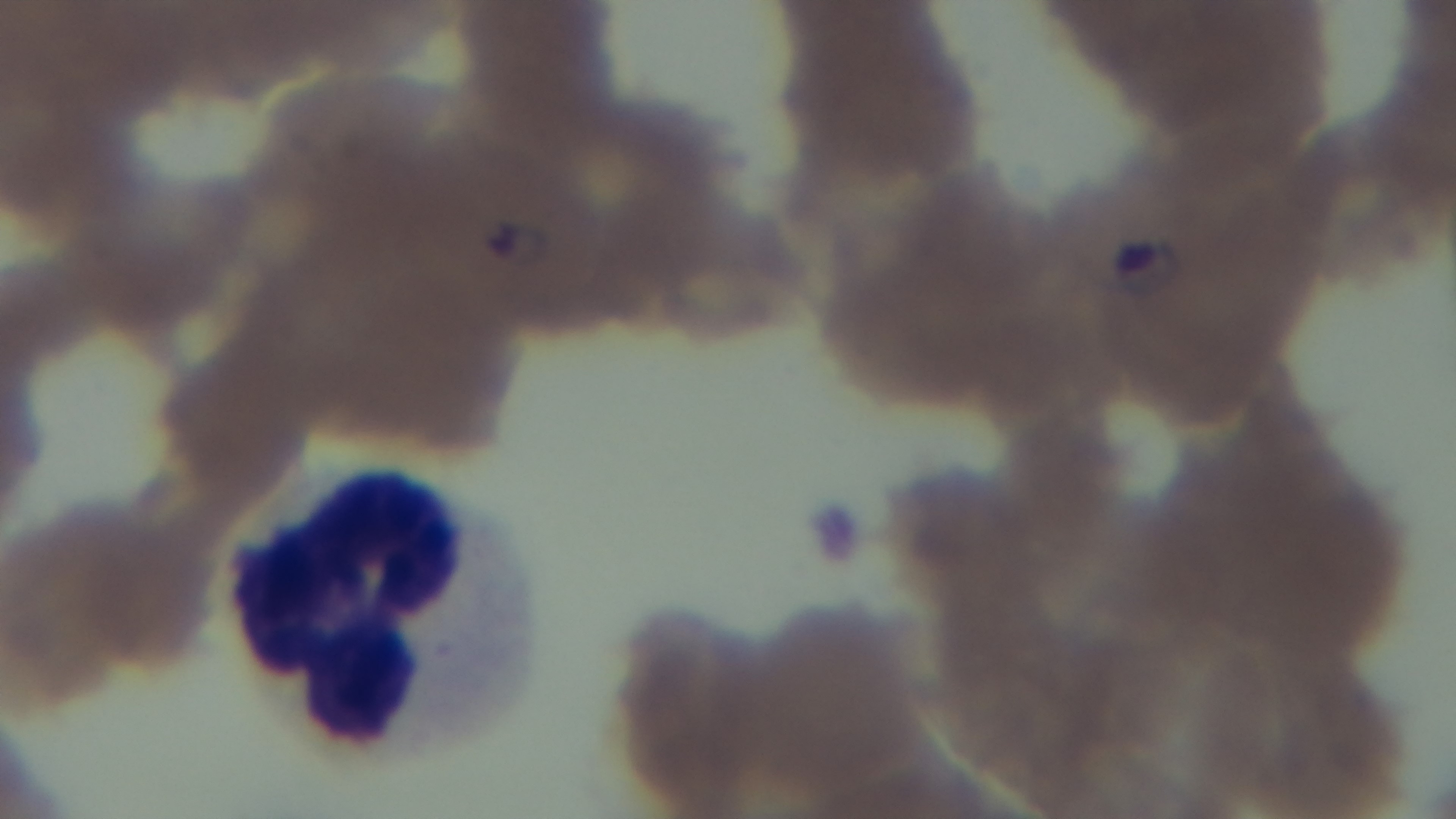

Summary:
  - Objective: 100x oil immersion
  - Malaria status: infected
  - Field of view: one from the slide
  - Stain: Giemsa
  - Preparation: thin blood film
  - Capture: mounted 4K digital camera
  - Modality: light microscopy